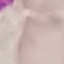
result = no malaria parasites seen
stain = Giemsa
capture = smartphone camera at the microscope eyepiece
preparation = thin blood smear
image type = automatically extracted cell patch, resized to 64 × 64 pixels